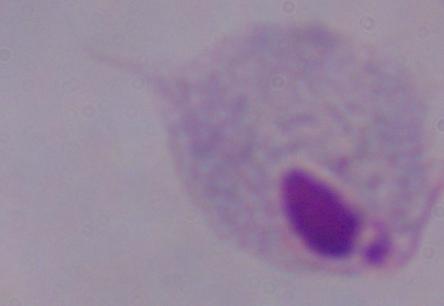
Summary:
  - Magnification: 1000x
  - Identification: trichomonad
  - Modality: micrograph